Locate and identify every blood parasite.
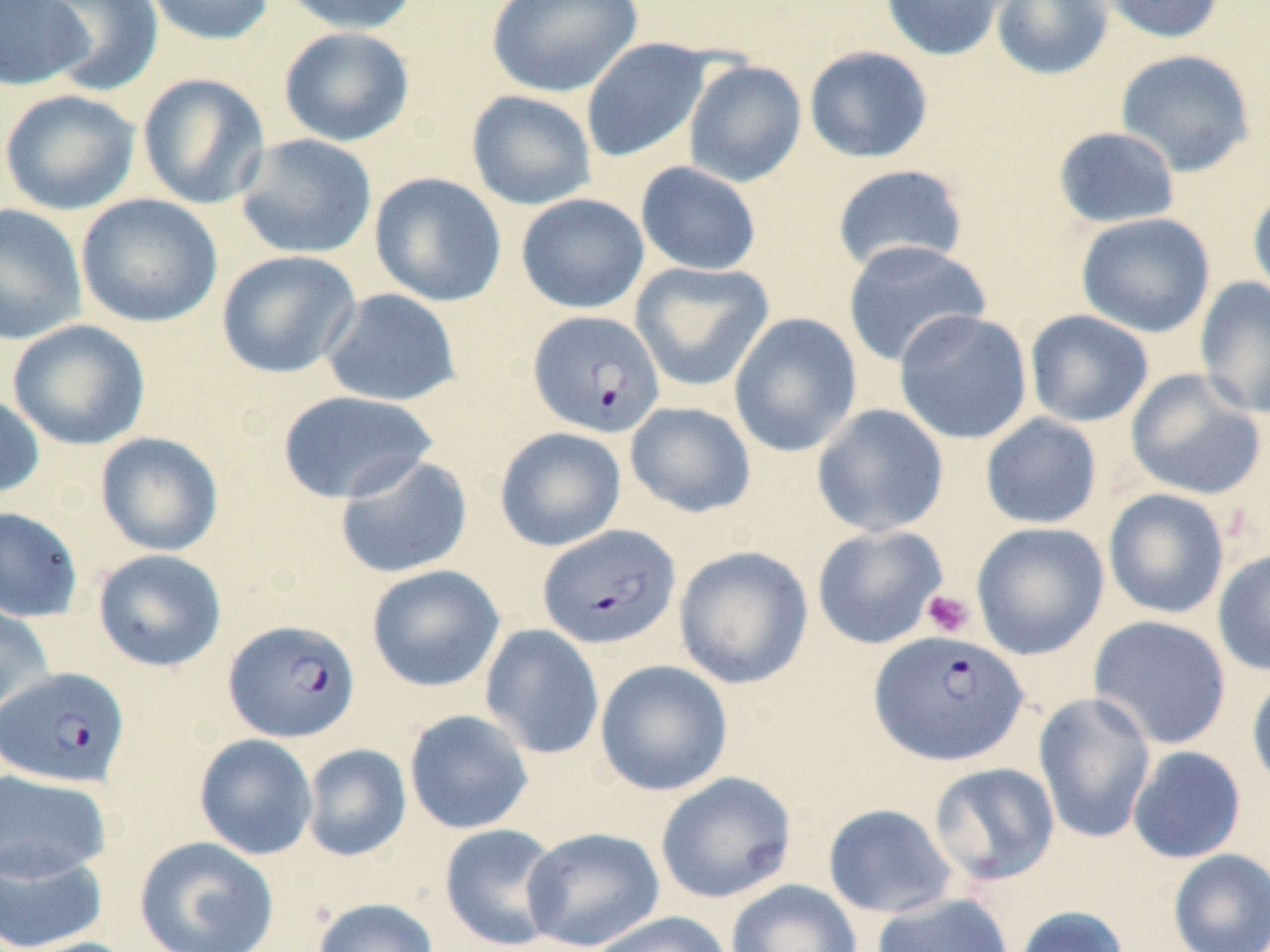
Approximate bounding boxes as (x1,y1)-(x2,y2) corner pairs in pixels.
Plasmodium falciparum-infected red blood cells: (528,310)-(665,438), (538,524)-(681,650), (223,619)-(360,743), (868,630)-(1029,766), (0,666)-(130,788).
No Plasmodium ovale, Plasmodium malariae, Plasmodium vivax, Babesia divergens, or Trypanosoma brucei observed.

Summary:
  - Uninfected red blood cell locations: (0,0)-(90,92), (35,0)-(164,96), (143,0)-(276,46), (280,0)-(421,35), (486,0)-(643,97), (880,0)-(1011,61), (991,0)-(1113,80), (1096,0)-(1226,44), (278,26)-(415,147), (581,38)-(713,163), (804,45)-(933,164), (1114,48)-(1256,177), (683,59)-(807,187), (137,72)-(271,210), (0,88)-(140,216), (465,90)-(597,211), (1052,126)-(1181,229), (234,133)-(377,260), (635,161)-(762,276), (831,164)-(968,275), (368,172)-(507,307), (1248,184)-(1270,304), (516,193)-(649,314), (75,194)-(223,328), (0,203)-(87,346), (1076,212)-(1216,338), (842,239)-(991,368), (216,250)-(362,379), (630,262)-(775,392), (1194,276)-(1270,420), (320,288)-(462,407), (893,309)-(1033,445), (1025,309)-(1154,428), (729,313)-(862,457), (8,319)-(151,451), (1125,368)-(1267,501), (276,390)-(438,504), (0,391)-(45,499), (625,401)-(756,518), (811,403)-(949,537), (980,413)-(1102,529), (494,427)-(627,552), (95,432)-(224,557), (334,455)-(473,579), (1103,489)-(1230,619), (0,506)-(84,623), (971,522)-(1110,660), (811,524)-(949,650), (673,545)-(814,690), (92,548)-(227,672), (1212,548)-(1270,676), (366,565)-(505,693), (0,602)-(56,716), (1088,615)-(1232,750), (480,624)-(604,760), (594,659)-(733,796), (1247,670)-(1270,794), (1033,691)-(1157,844), (404,709)-(534,834), (194,734)-(319,860), (301,744)-(412,862), (1128,746)-(1246,863), (928,762)-(1061,886), (0,769)-(112,882), (655,772)-(797,904), (823,804)-(957,918), (439,823)-(564,951), (521,826)-(665,952), (134,835)-(280,952), (0,843)-(108,952), (1168,848)-(1270,952), (725,879)-(862,952), (871,892)-(1015,952), (312,897)-(439,952), (1012,905)-(1130,952), (586,910)-(734,952), (14,936)-(144,952)
  - Platelet locations: (921,589)-(976,639)
  - Slide-level diagnosis: Plasmodium falciparum
  - Preparation: thin blood film
  - Modality: light microscopy
  - Magnification: 1000x
  - Stain: May-Grünwald-Giemsa
  - Image size: 1270×952 pixels
  - Field of view: one of a larger specimen